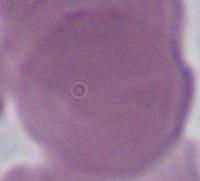 1000x magnification. An erythrocyte is shown. Photomicrograph.